Assess the morphology of the erythrocytes.
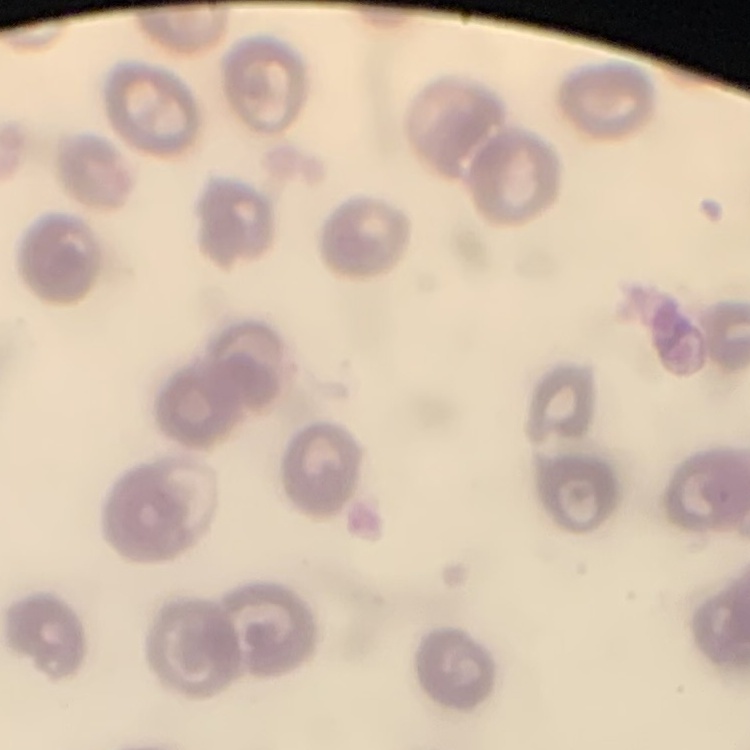
They show no rouleaux formation.

Summary:
  - Preparation: thin peripheral smear
  - Image type: square crop of a larger photomicrograph
  - Stain: Field's or Giemsa